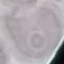
malaria status = uninfected
stain = Giemsa
preparation = thin blood smear
capture = smartphone camera at the microscope eyepiece
image type = cell patch, automatically extracted from a larger field of view and resized to 64 × 64 pixels